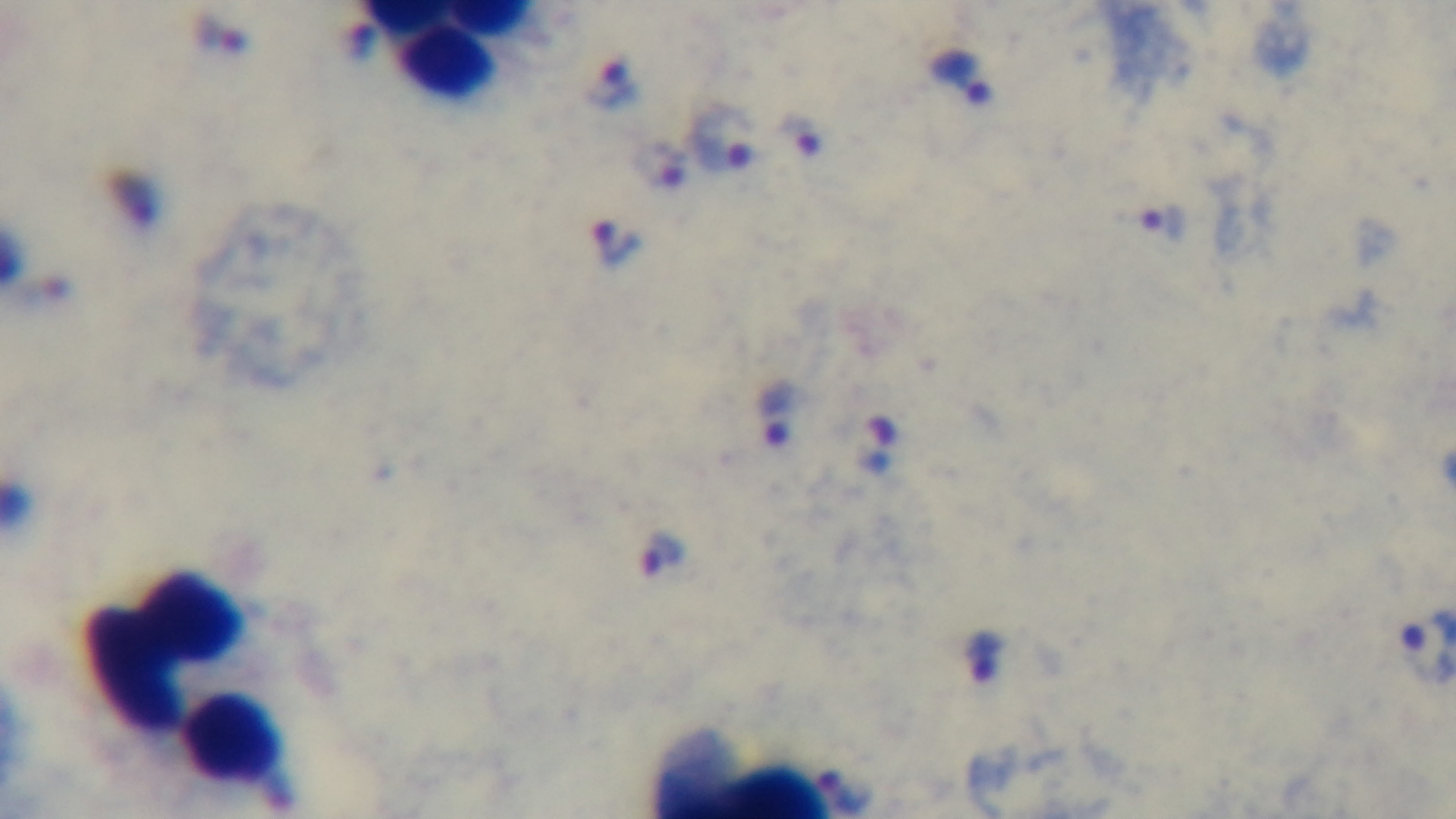
{
  "preparation": "thick",
  "malaria_status": "infected",
  "stain": "Giemsa",
  "objective": "100x oil immersion",
  "modality": "light microscopy",
  "field_of_view": "single",
  "capture": "mounted 4K digital camera"
}